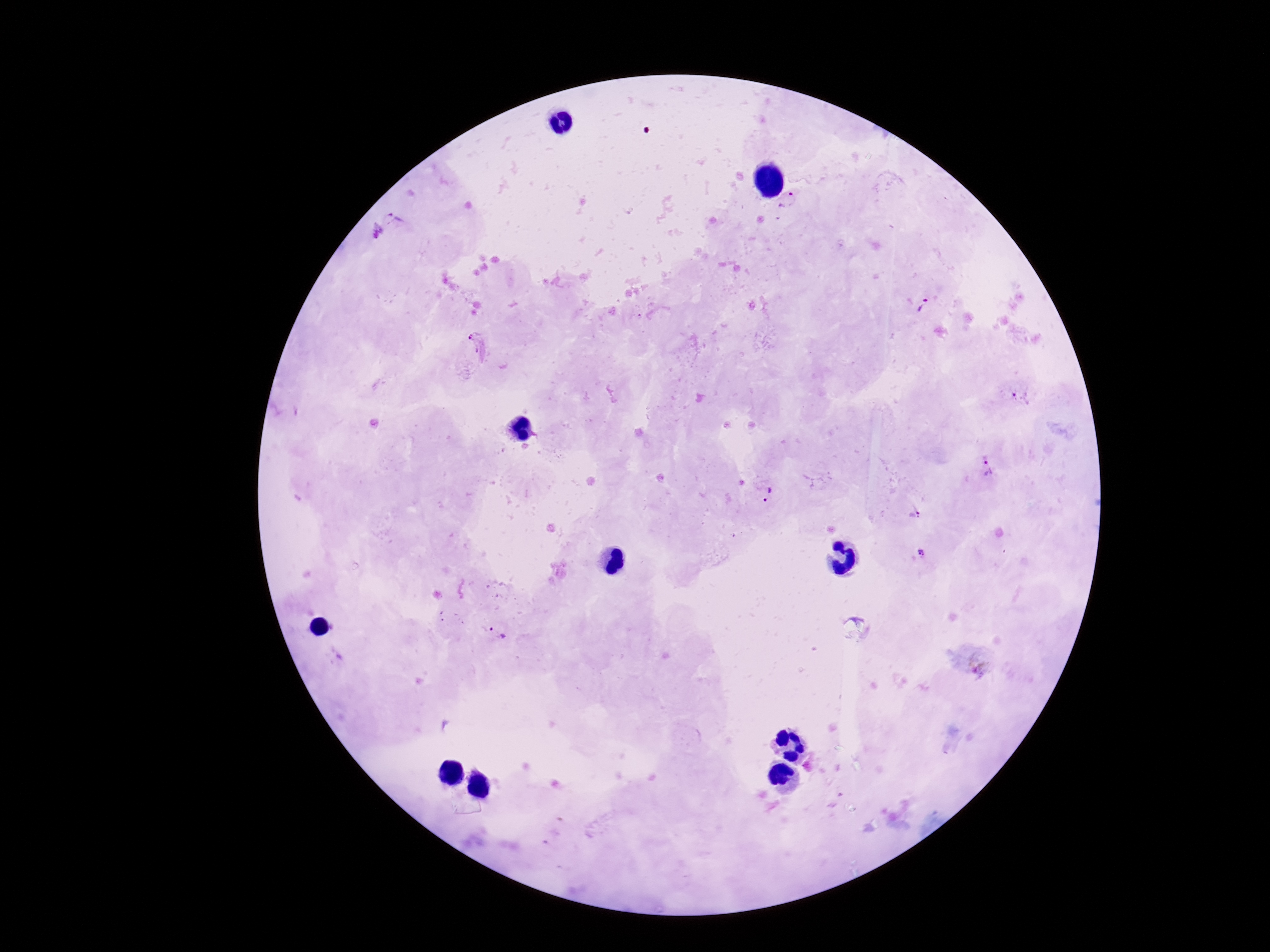

stain: Giemsa
capture: smartphone camera through the microscope eyepiece
magnification: 100x
patient_malaria_status: positive
field_of_view: single
preparation: thick peripheral-blood smear
plasmodium_parasite_locations: 'approximate centers as [x, y] in pixels: [789, 202], [394, 217], [375, 232], [923, 307], [480, 346], [1020, 398], [987, 467], [766, 495], [914, 513], [921, 553], [496, 632]'
image_size: 1270×952 pixels